Name the blood parasite species.
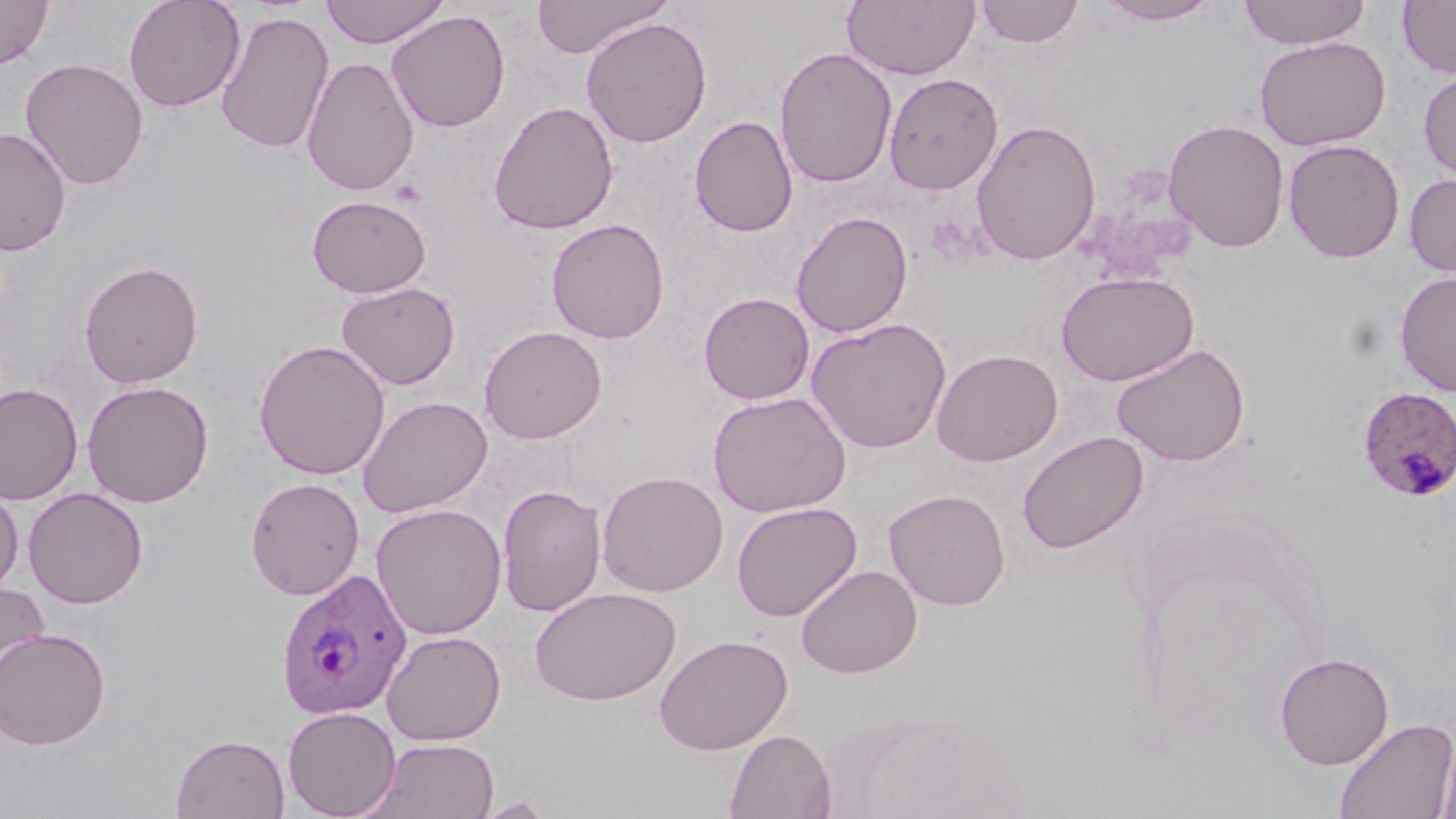
Plasmodium ovale.

Summary:
  - Coordinate format: approximate bounding boxes as (x1,y1)-(x2,y2) corner pairs in pixels
  - Plasmodium ovale-infected red blood cell locations: (1357,386)-(1455,501), (275,568)-(412,719)
  - Platelet locations: (389,178)-(427,207)
  - Uninfected red blood cell locations: (0,0)-(54,70), (123,0)-(246,112), (320,0)-(450,48), (530,0)-(671,58), (842,0)-(980,79), (975,0)-(1084,47), (1097,0)-(1223,26), (1238,0)-(1370,49), (1398,0)-(1456,79), (215,9)-(335,154), (386,10)-(510,132), (581,16)-(712,148), (1255,36)-(1391,151), (774,47)-(898,188), (302,55)-(420,196), (20,57)-(149,189), (1418,69)-(1456,180), (883,72)-(1004,195), (488,101)-(618,235), (689,115)-(798,237), (971,119)-(1102,265), (1163,119)-(1289,252), (0,127)-(71,256), (1283,139)-(1405,262), (1404,172)-(1456,279), (307,194)-(432,297), (792,211)-(913,338), (546,218)-(670,344), (79,260)-(204,388), (1056,270)-(1199,386), (1394,270)-(1456,397), (335,281)-(460,390), (699,292)-(814,405), (807,318)-(952,453), (479,325)-(607,443), (254,339)-(391,480), (1112,343)-(1250,467), (932,348)-(1063,467), (82,380)-(214,508), (0,383)-(83,505), (707,391)-(852,517), (357,395)-(493,517), (1018,431)-(1149,554), (597,469)-(728,597), (245,477)-(365,600), (497,483)-(606,617), (0,486)-(24,595), (23,487)-(148,609), (884,488)-(1011,610), (731,501)-(863,622), (371,502)-(508,639), (795,563)-(923,678), (0,578)-(50,693), (529,586)-(681,705), (0,626)-(111,750), (381,629)-(507,745), (655,634)-(794,755), (1275,652)-(1394,769), (283,706)-(401,818), (1333,715)-(1455,819), (725,728)-(836,819), (1437,731)-(1456,819), (170,732)-(290,818), (366,737)-(500,819), (473,796)-(556,818)
  - Field of view: one of a larger specimen
  - Magnification: 1000x
  - Stain: May-Grünwald-Giemsa
  - Image size: 1456×819 pixels
  - Preparation: thin blood film
  - Modality: light microscopy